Assess this cell for malaria.
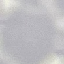
Uninfected.

{
  "stain": "Giemsa",
  "preparation": "thin blood film",
  "image_type": "cell patch, automatically extracted from a larger field of view and resized to 64 × 64 pixels",
  "capture": "smartphone camera at the microscope eyepiece"
}